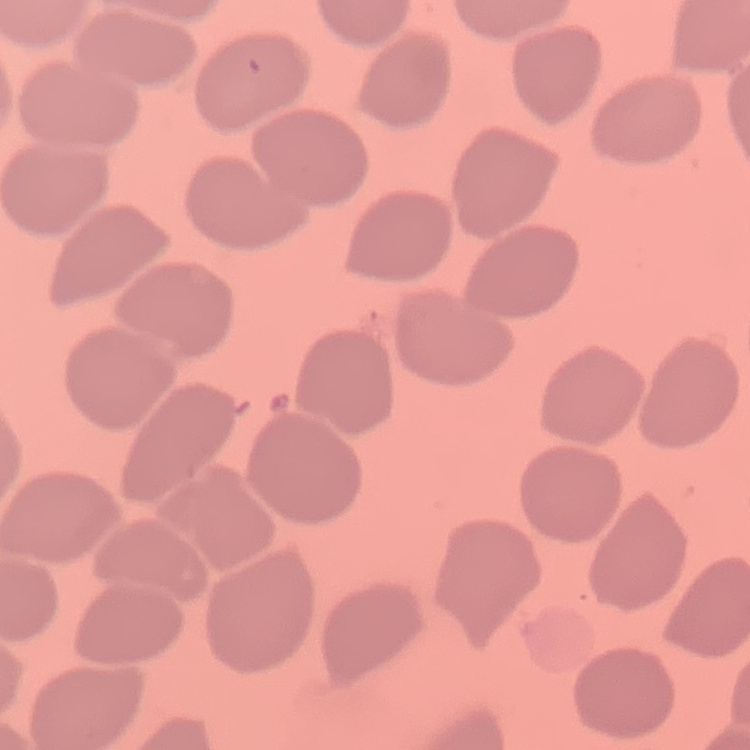 The red blood cells show no rouleaux formation. Thin peripheral smear. Stained with either Field's or Giemsa. One tile cut from a larger photomicrograph.